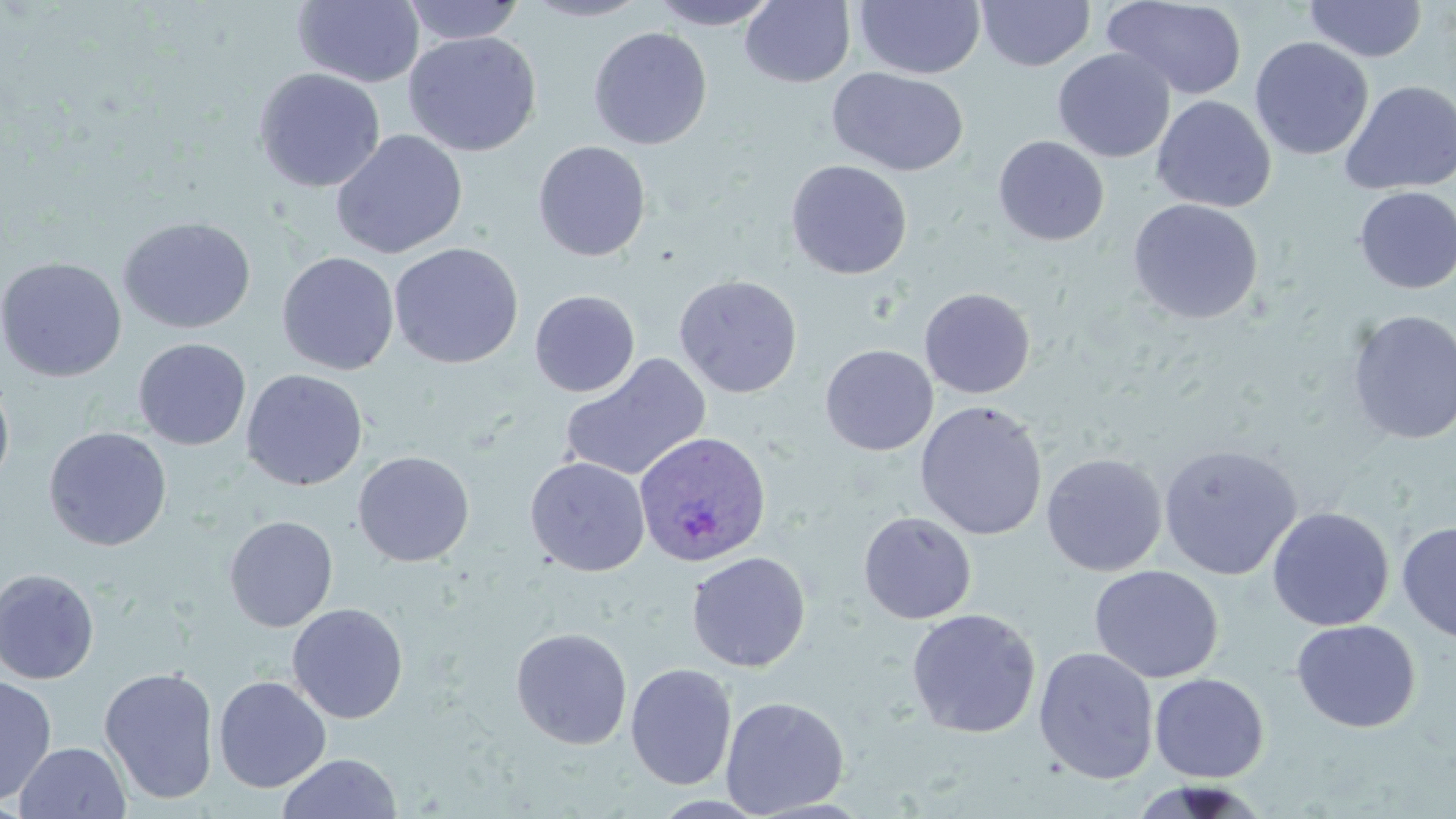
Approximate bounding boxes as [x1, y1, x2, y2] in pixels. Plasmodium ovale-infected red blood cell locations: [634, 431, 772, 567]. Uninfected red blood cell locations: [292, 0, 425, 88], [521, 0, 652, 22], [651, 0, 779, 30], [740, 0, 856, 88], [854, 0, 985, 79], [976, 0, 1095, 71], [1102, 0, 1248, 100], [401, 1, 526, 44], [1303, 1, 1427, 62], [589, 26, 712, 150], [403, 31, 542, 157], [1249, 36, 1374, 161], [1052, 48, 1176, 163], [253, 67, 386, 192], [828, 67, 969, 177], [1340, 80, 1456, 196], [1151, 95, 1277, 214], [330, 129, 468, 259], [993, 135, 1109, 247], [533, 141, 651, 262], [786, 160, 912, 279], [1353, 186, 1456, 294], [1128, 198, 1264, 325], [118, 216, 256, 334], [388, 242, 524, 369], [277, 251, 400, 375], [0, 257, 126, 382], [674, 274, 803, 398], [918, 287, 1036, 398], [529, 290, 640, 397], [1346, 309, 1456, 445], [133, 338, 252, 450], [820, 344, 938, 456], [559, 353, 713, 482], [241, 369, 369, 491], [0, 370, 15, 495], [914, 400, 1049, 540], [44, 426, 172, 551], [1158, 442, 1302, 580], [353, 450, 475, 566], [1041, 452, 1167, 577], [525, 456, 650, 576], [1266, 506, 1394, 631], [858, 511, 977, 624], [224, 515, 338, 632], [1396, 520, 1456, 644], [686, 551, 811, 671], [1089, 564, 1223, 683], [0, 568, 100, 685], [287, 603, 408, 723], [906, 608, 1041, 738], [1291, 619, 1420, 733], [510, 627, 633, 750], [1033, 647, 1159, 785], [625, 663, 737, 791], [99, 666, 219, 805], [1150, 673, 1269, 783], [0, 674, 58, 806], [213, 675, 332, 793], [720, 695, 849, 817], [13, 742, 131, 818], [276, 752, 403, 818], [1129, 780, 1270, 819]. Slide-level diagnosis: Plasmodium ovale. Optical microscopy. One field of a larger specimen. Image is 1456×819 pixels. May-Grünwald-Giemsa stain. Thin blood smear. Captured at 1000x magnification.